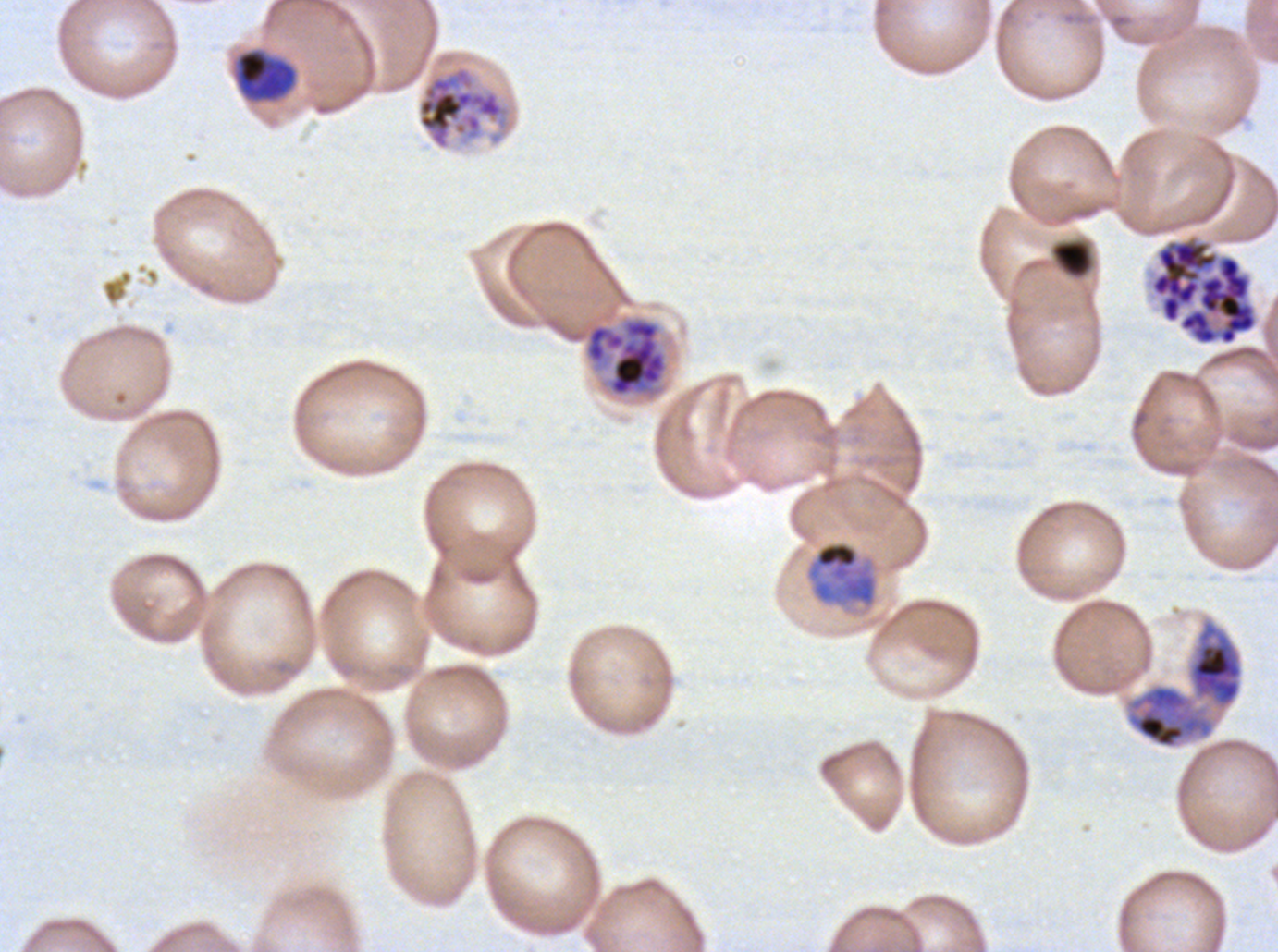

Approximate bounding boxes as {x1, y1, x2, y2} in pixels.
Summary:
  - Late schizont locations: {416, 65, 511, 151}, {545, 315, 669, 400}
  - Mid trophozoite locations: {235, 48, 298, 103}
  - Segmenter locations: {1149, 234, 1259, 347}
  - Early schizont locations: {1123, 616, 1245, 751}
  - Late trophozoite locations: {805, 540, 879, 610}
  - Debris locations: {1051, 239, 1093, 278}
  - Life-cycle stages observed: mid trophozoite, late trophozoite, early schizont, late schizont, segmenter
  - Stain: Giemsa
  - Preparation: thin blood film
  - Field of view: one sub-image of a larger composite
  - Specimen: ex-vivo P. falciparum culture from a patient in The Gambia, grown for 24 to 48 hours
  - Image size: 1278×952 pixels